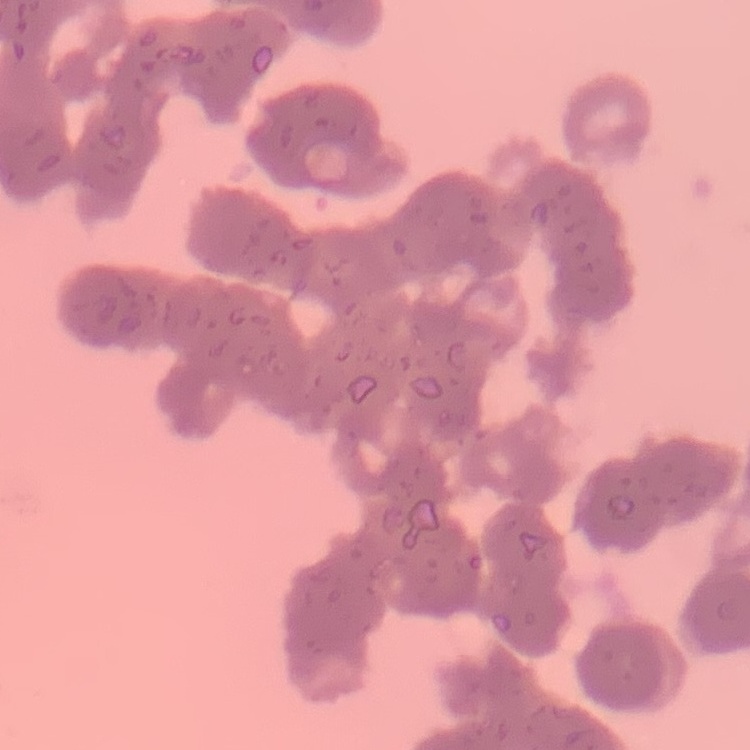
The erythrocytes exhibit rouleaux formation. Thin peripheral smear. Stained with either Field's or Giemsa. One tile cut from a larger photomicrograph.